Name the parasite shown.
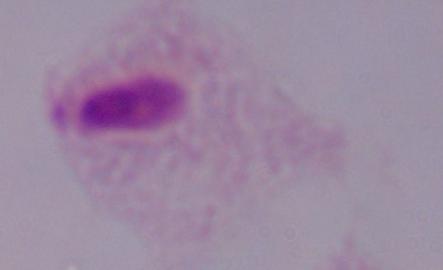
A trichomonad.

Summary:
  - Magnification: 1000x
  - Modality: photomicrograph